Report the malaria status of this cell.
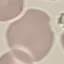

It is uninfected.

Giemsa stain. Photographed with a smartphone camera at the microscope eyepiece. Thin blood smear. Cell patch, automatically extracted from a larger field of view and resized to 64 × 64 pixels.